Classify this cell by malaria status.
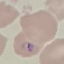

Parasitized.

Summary:
  - Image type: cell patch, automatically extracted from a larger field of view and resized to 64 × 64 pixels
  - Stain: Giemsa
  - Preparation: thin blood film
  - Capture: smartphone through the microscope eyepiece